Report the malaria status of this cell.
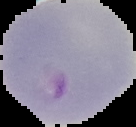

It is parasitized.

From a thin blood smear. Cell region segmented out of the field of view; the surrounding area is masked to black. Image is 136×127 pixels.